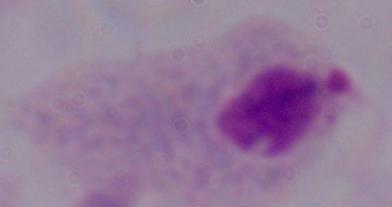 A trichomonad is seen. 1000x magnification. Photomicrograph.